State which parasite is depicted.
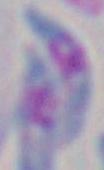

This is Toxoplasma gondii.

modality = photomicrograph
magnification = 1000x